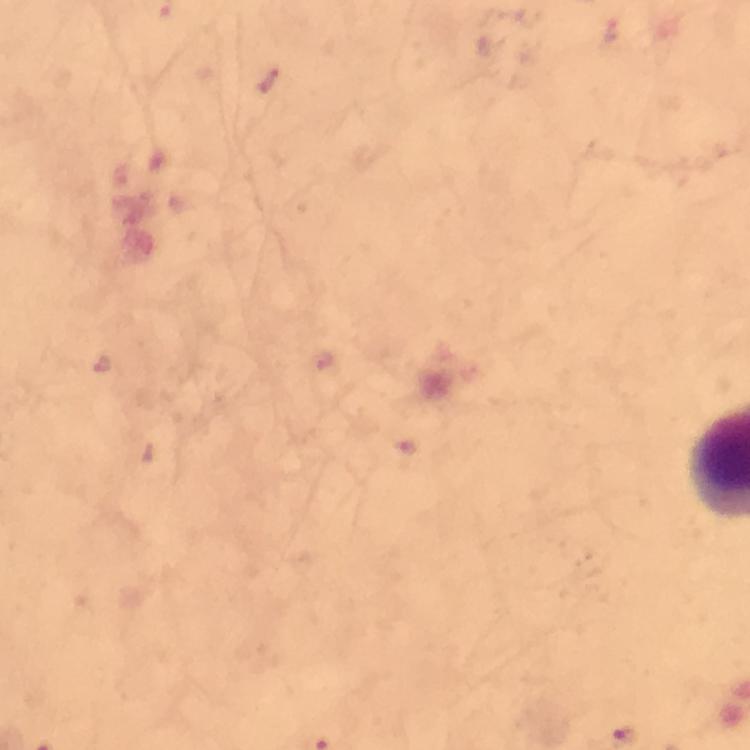

Approximate centers as [x, y] in pixels.
Summary:
  - Malaria parasite locations: [268, 82], [323, 362], [100, 365]
  - Preparation: thick blood smear
  - Context: from a diagnostic examination for malaria
  - Cropped from: a single field of view
  - Image size: 750×750 pixels
  - Magnification: 100x
  - Immersion oil: used
  - Capture: smartphone camera through the microscope
  - Stain: Giemsa